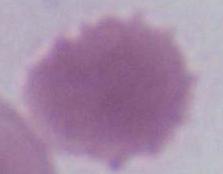

{
  "magnification": "1000x",
  "modality": "micrograph",
  "identification": "red blood cell"
}